Classify this cell by malaria status.
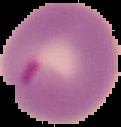
Parasitized.

Summary:
  - Image type: cell region segmented out of the field of view; surrounding area masked to black
  - Image size: 121×127 pixels
  - Preparation: thin blood film